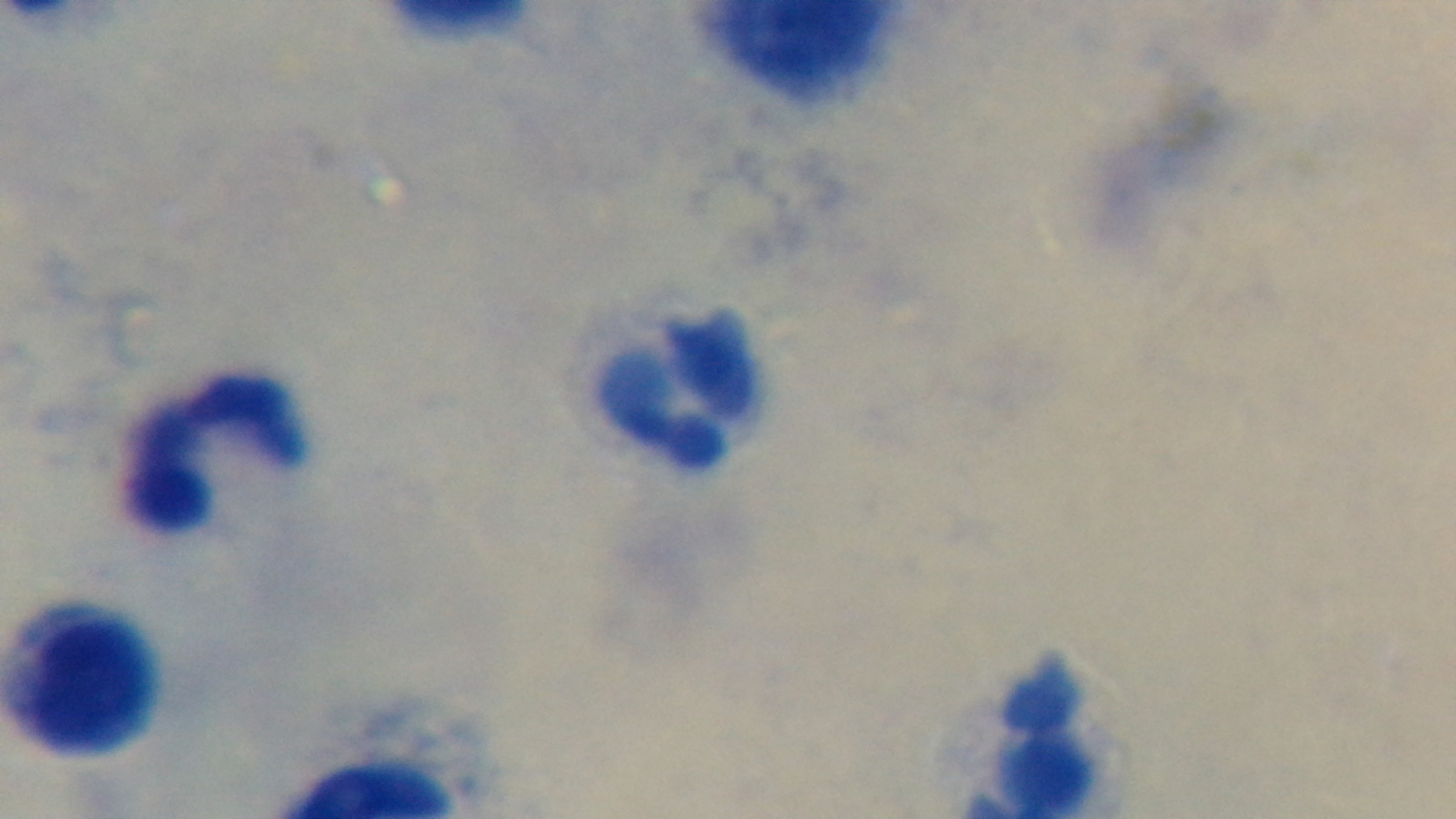
field of view = one from the slide
objective = 100x oil immersion
stain = Giemsa
capture = mounted 4K digital camera
malaria status = negative
modality = light microscopy
preparation = thick